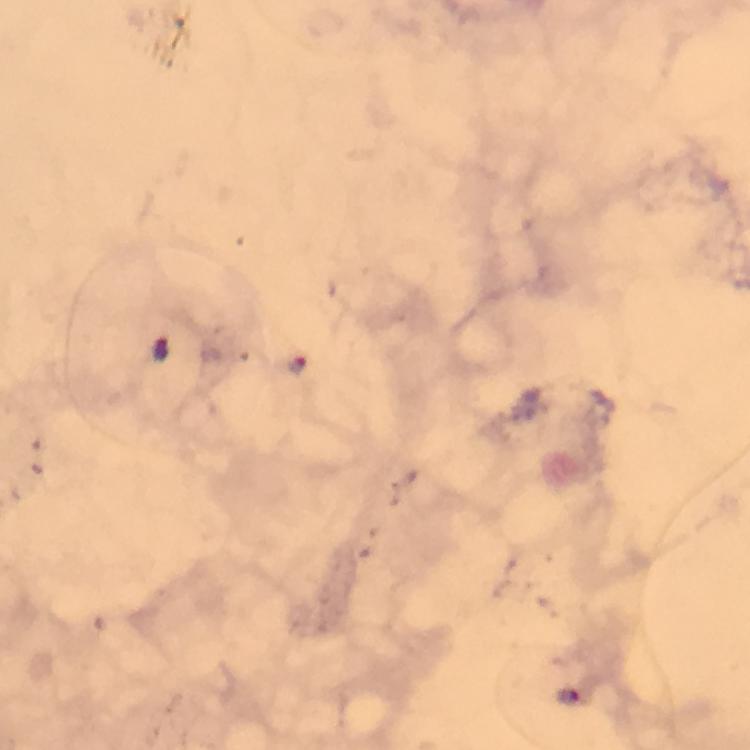

Approximate centers as (x, y) in pixels. Malaria parasite locations: (303, 367). Immersion oil applied. Image is 750×750 pixels. Photographed with a smartphone mounted on the microscope. A crop from one field of view. Giemsa stain. From a diagnostic examination for malaria. Thick blood smear. At 100x magnification.